Classify this cell by malaria status.
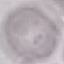
It is uninfected.

Summary:
  - Stain: Giemsa
  - Image type: cell patch, automatically extracted from a larger field of view and resized to 64 × 64 pixels
  - Preparation: thin smear
  - Capture: smartphone through the microscope eyepiece